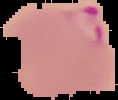
preparation = thin blood film
result = Plasmodium parasites detected
image size = 118×100 pixels
image type = segmented cell region on a black background